Locate every blood parasite and identify its species.
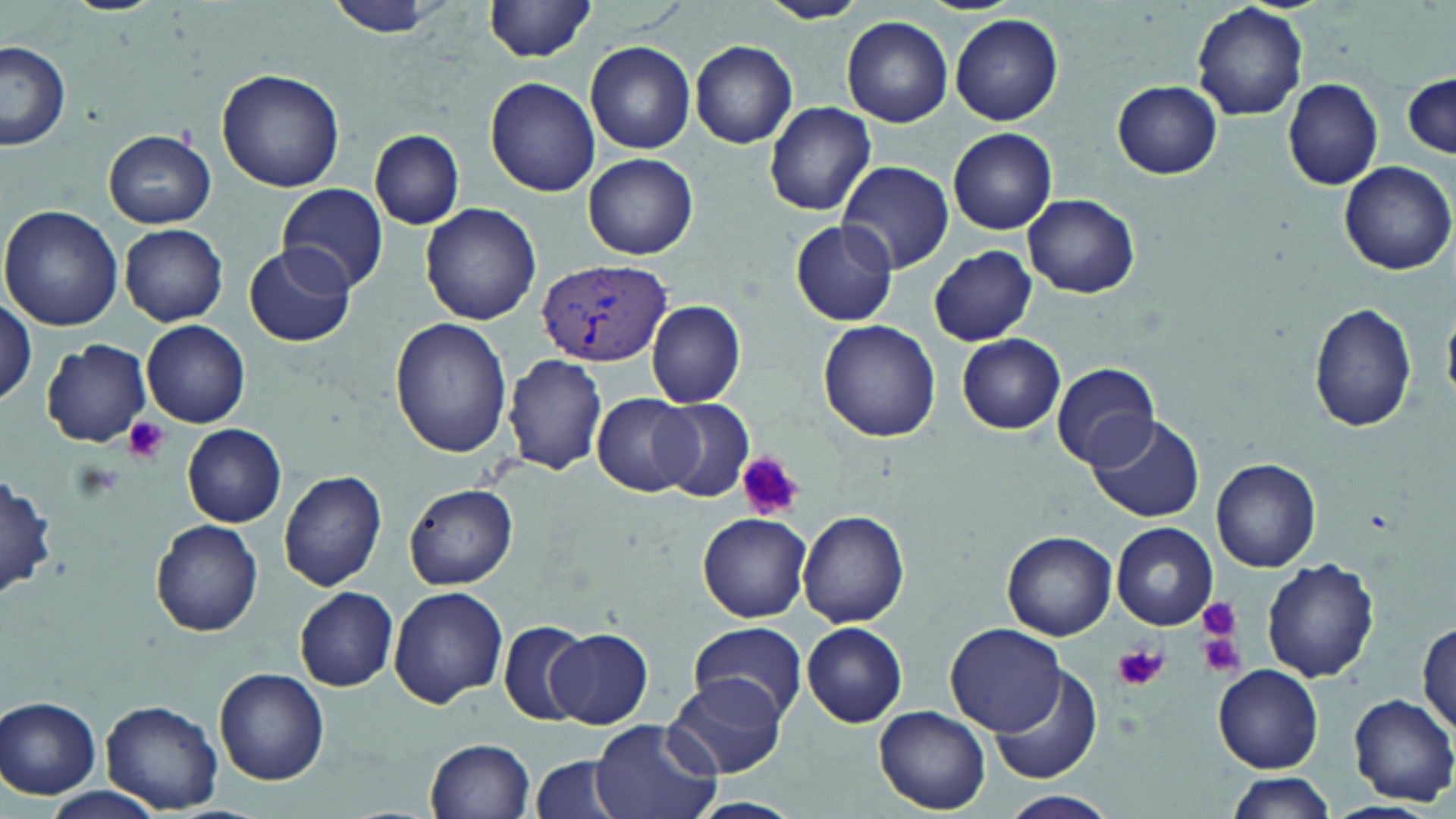

Approximate bounding boxes as (x1, y1, x2, y2) in pixels.
Plasmodium vivax-infected red blood cells: (535, 256, 670, 368).
No Plasmodium falciparum, Plasmodium ovale, Plasmodium malariae, Babesia divergens, or Trypanosoma brucei observed.

Uninfected red blood cell locations: (484, 0, 600, 63), (760, 0, 868, 24), (326, 2, 443, 39), (1192, 2, 1307, 119), (951, 13, 1064, 125), (842, 15, 954, 127), (586, 40, 696, 153), (690, 40, 798, 149), (1, 42, 71, 151), (218, 68, 344, 192), (1402, 74, 1456, 158), (486, 76, 600, 196), (1282, 76, 1385, 189), (1112, 80, 1222, 179), (765, 101, 877, 216), (948, 128, 1057, 235), (105, 130, 216, 227), (370, 130, 464, 229), (584, 153, 697, 258), (834, 160, 956, 275), (1339, 161, 1454, 276), (277, 184, 389, 294), (1023, 195, 1138, 297), (421, 203, 541, 325), (1, 206, 125, 333), (790, 221, 899, 325), (120, 224, 229, 326), (241, 243, 356, 349), (929, 244, 1035, 345), (0, 292, 35, 409), (646, 300, 746, 406), (1308, 303, 1416, 433), (390, 317, 512, 457), (141, 320, 250, 428), (818, 320, 941, 442), (957, 334, 1066, 433), (42, 339, 151, 447), (503, 354, 609, 475), (1049, 363, 1162, 468), (593, 394, 695, 498), (651, 397, 755, 503), (1084, 413, 1203, 523), (183, 425, 286, 526), (1211, 455, 1321, 572), (1, 468, 55, 603), (278, 469, 387, 590), (406, 485, 517, 589), (798, 509, 910, 627), (699, 512, 812, 621), (151, 519, 263, 637), (1113, 523, 1217, 631), (1002, 532, 1116, 641), (1263, 559, 1378, 682), (388, 586, 506, 709), (292, 587, 399, 691), (497, 618, 592, 725), (1416, 620, 1455, 734), (686, 621, 808, 724), (801, 621, 908, 727), (946, 622, 1067, 734), (545, 628, 652, 728), (1215, 665, 1323, 771), (988, 668, 1101, 784), (215, 669, 330, 785), (667, 673, 786, 778), (1344, 693, 1456, 805), (1, 697, 102, 798), (102, 699, 223, 813), (875, 706, 991, 814), (588, 719, 723, 819), (425, 738, 535, 819), (531, 755, 632, 819), (1223, 772, 1336, 818), (41, 787, 162, 819), (999, 790, 1119, 819), (1319, 801, 1438, 819). Platelet locations: (122, 416, 170, 464), (738, 453, 803, 519), (1198, 597, 1241, 638), (1198, 632, 1245, 677), (1115, 645, 1167, 692). Slide-level diagnosis: Plasmodium vivax. Light microscopy. One field of a larger specimen. Thin blood film. May-Grünwald-Giemsa-stained preparation. Captured at 1000x magnification. Image is 1456×819 pixels.